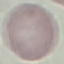

Result: no malaria parasites detected. Thin smear of blood. Cell patch, automatically extracted from a larger field of view and resized to 64 × 64 pixels. Photographed with a smartphone camera at the microscope eyepiece. Giemsa-stained preparation.